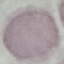
Result: no malaria parasites seen. Photographed with a smartphone camera at the microscope eyepiece. Automatically extracted cell patch, resized to 64 × 64 pixels. Thin blood film. Giemsa-stained preparation.